Identify the parasite.
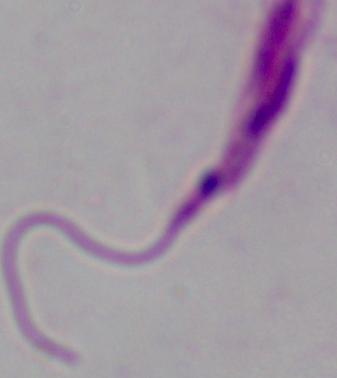

This is Leishmania.

Captured at 1000x magnification. Micrograph.